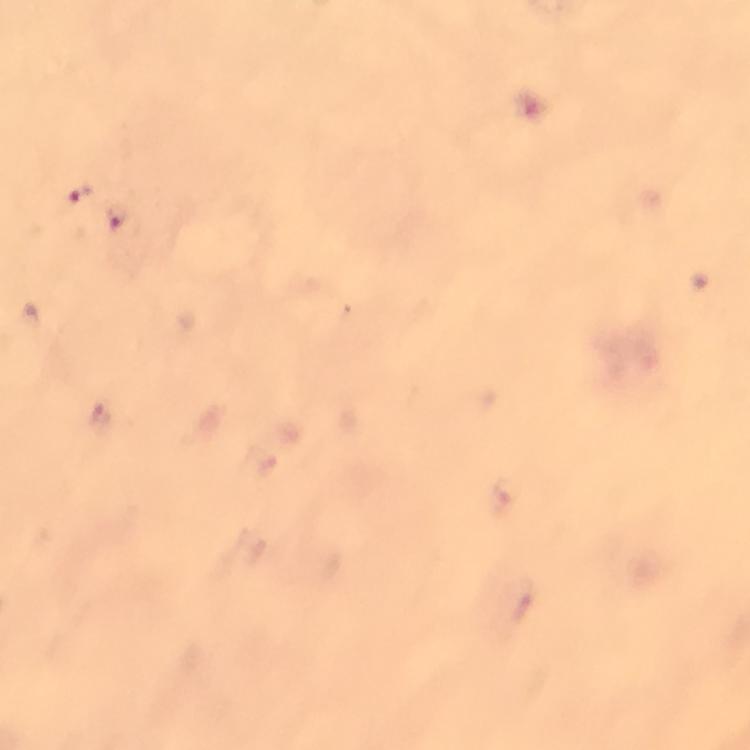

preparation = thick blood smear
magnification = 100x
malaria parasite locations = approximate centers as {x, y} in pixels: {75, 194}, {118, 220}
context = from a diagnostic examination for malaria
capture = smartphone mounted on the microscope
cropped from = one field of view
stain = Giemsa
image size = 750×750 pixels
immersion oil = applied